Assess this cell for malaria.
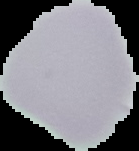

It is uninfected.

{
  "preparation": "thin blood smear",
  "image_size": "139×151 pixels",
  "image_type": "segmented cell region on a black background"
}